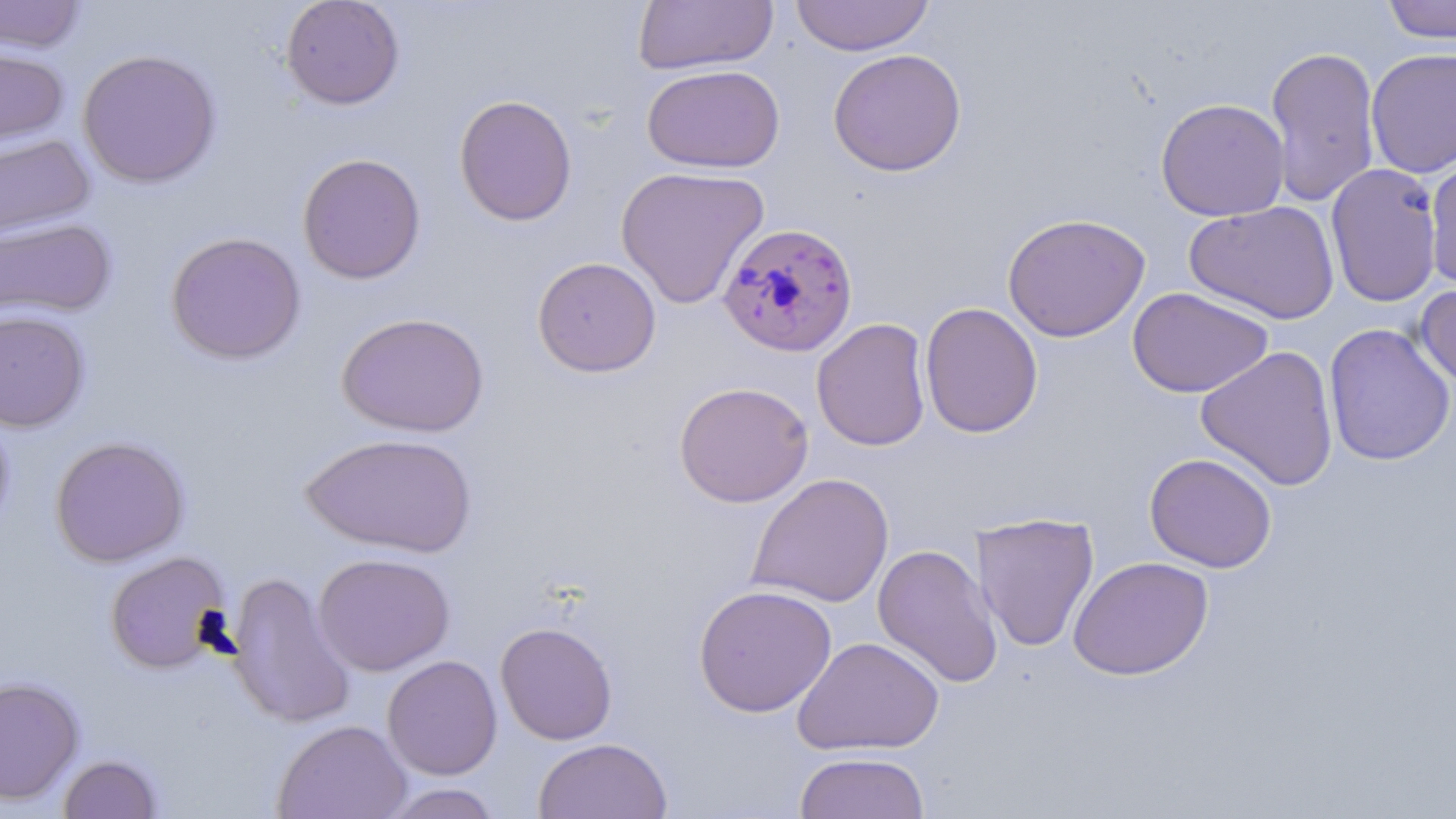
Approximate bounding boxes as named x1/y1/x2/y2 corners in pixels. Plasmodium falciparum-infected red blood cell locations: (x1=717, y1=221, x2=858, y2=358). Uninfected red blood cell locations: (x1=0, y1=0, x2=87, y2=54), (x1=280, y1=0, x2=405, y2=110), (x1=789, y1=0, x2=935, y2=56), (x1=1380, y1=0, x2=1456, y2=45), (x1=633, y1=1, x2=778, y2=75), (x1=0, y1=44, x2=69, y2=153), (x1=1265, y1=45, x2=1381, y2=207), (x1=827, y1=48, x2=967, y2=176), (x1=1365, y1=48, x2=1456, y2=178), (x1=77, y1=49, x2=222, y2=188), (x1=642, y1=64, x2=784, y2=173), (x1=454, y1=94, x2=578, y2=226), (x1=1155, y1=97, x2=1290, y2=222), (x1=0, y1=133, x2=95, y2=243), (x1=296, y1=152, x2=426, y2=285), (x1=1424, y1=152, x2=1456, y2=290), (x1=1325, y1=162, x2=1443, y2=308), (x1=616, y1=166, x2=770, y2=309), (x1=1184, y1=200, x2=1340, y2=324), (x1=1002, y1=212, x2=1151, y2=342), (x1=0, y1=217, x2=117, y2=322), (x1=165, y1=231, x2=306, y2=364), (x1=531, y1=257, x2=662, y2=378), (x1=1415, y1=282, x2=1456, y2=389), (x1=1127, y1=287, x2=1273, y2=398), (x1=919, y1=302, x2=1043, y2=438), (x1=0, y1=308, x2=91, y2=433), (x1=337, y1=311, x2=490, y2=437), (x1=811, y1=318, x2=932, y2=452), (x1=1323, y1=322, x2=1455, y2=466), (x1=1196, y1=345, x2=1340, y2=491), (x1=674, y1=381, x2=813, y2=507), (x1=0, y1=405, x2=15, y2=545), (x1=300, y1=432, x2=478, y2=557), (x1=50, y1=435, x2=190, y2=567), (x1=1144, y1=452, x2=1277, y2=573), (x1=747, y1=473, x2=894, y2=608), (x1=971, y1=512, x2=1099, y2=652), (x1=872, y1=543, x2=1003, y2=689), (x1=104, y1=551, x2=232, y2=674), (x1=312, y1=552, x2=455, y2=676), (x1=1068, y1=556, x2=1214, y2=681), (x1=226, y1=571, x2=356, y2=729), (x1=693, y1=584, x2=837, y2=718), (x1=495, y1=621, x2=618, y2=745), (x1=792, y1=636, x2=944, y2=756), (x1=382, y1=655, x2=503, y2=780), (x1=0, y1=676, x2=84, y2=806), (x1=273, y1=719, x2=412, y2=819), (x1=533, y1=737, x2=672, y2=819), (x1=794, y1=751, x2=930, y2=818), (x1=57, y1=754, x2=163, y2=819), (x1=377, y1=783, x2=505, y2=819). Slide-level diagnosis: Plasmodium falciparum. Optical microscopy. Captured at 1000x magnification. Single field of view. May-Grünwald-Giemsa stain. Thin blood smear. Image is 1456×819 pixels.